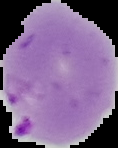 Image is 118×148 pixels. Result: malaria parasites detected. From a thin blood film. The area outside the segmented cell region is set to black.